Report the malaria status of this cell.
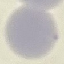
It is uninfected.

Giemsa-stained preparation. Thin blood film. Automatically extracted cell patch, resized to 64 × 64 pixels. Photographed with a smartphone camera at the microscope eyepiece.